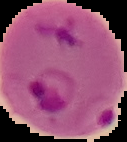 Result: Plasmodium parasites identified. Image is 127×142 pixels. From a thin blood film. The area outside the segmented cell region is set to black.